State which parasite is depicted.
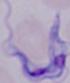
This is a trypanosome.

Captured at 1000x magnification. Micrograph.